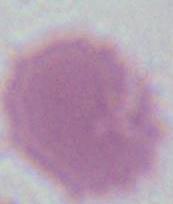 Photomicrograph. Captured at 1000x magnification. An erythrocyte is shown.